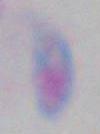

Summary:
  - Magnification: 1000x
  - Modality: micrograph
  - Identification: Toxoplasma gondii